Evaluate for malaria.
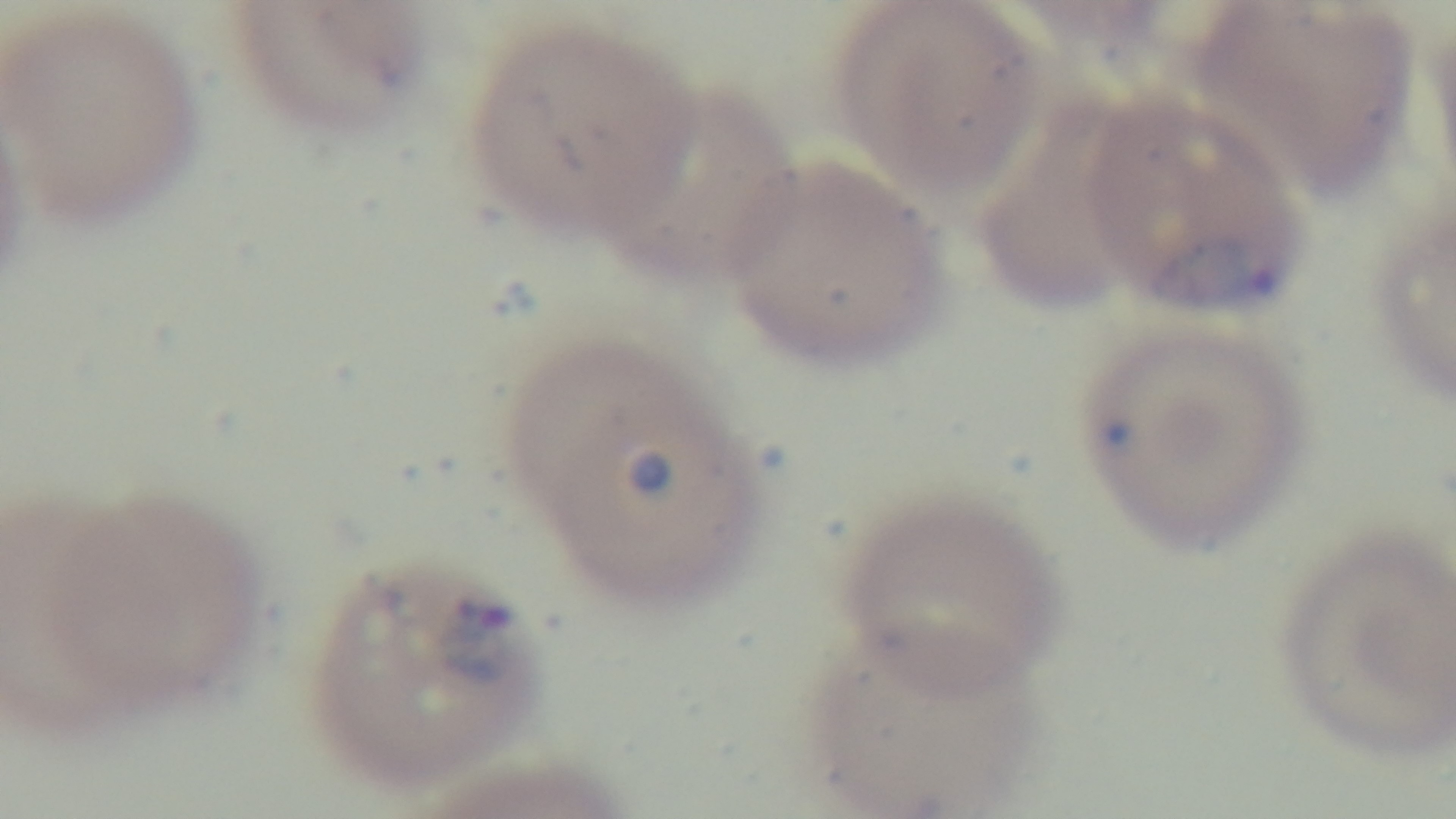
Infected.

objective = 100x oil immersion
capture = mounted 4K digital camera
preparation = thin blood film
field of view = single
stain = Giemsa
modality = light microscopy